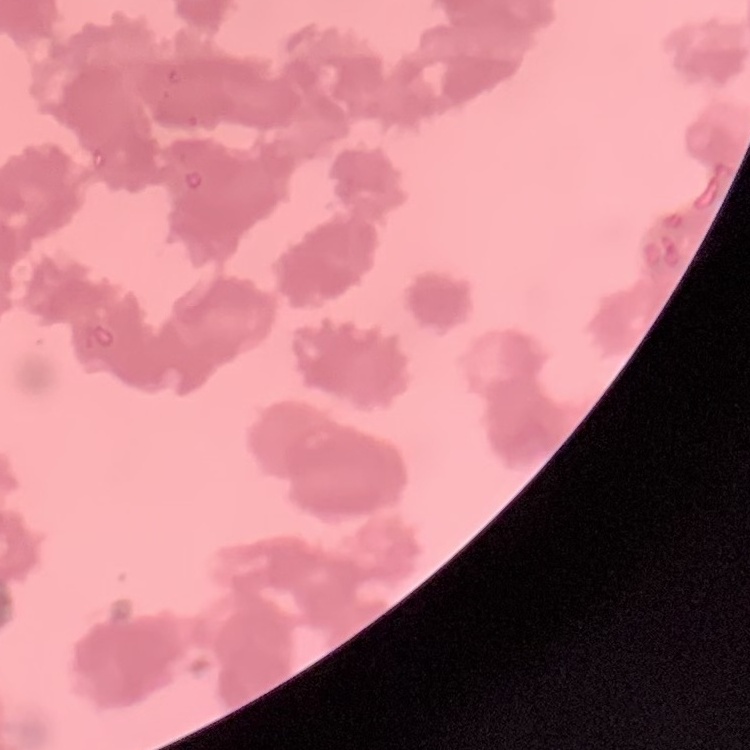 The erythrocytes show rouleaux formation. Field's or Giemsa stain. Thin blood smear. One tile cut from a larger photomicrograph.